Classify this cell by malaria status.
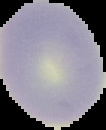

Uninfected.

image_type: cell region segmented out of the field of view; surrounding area masked to black
preparation: thin blood smear
image_size: 106×130 pixels